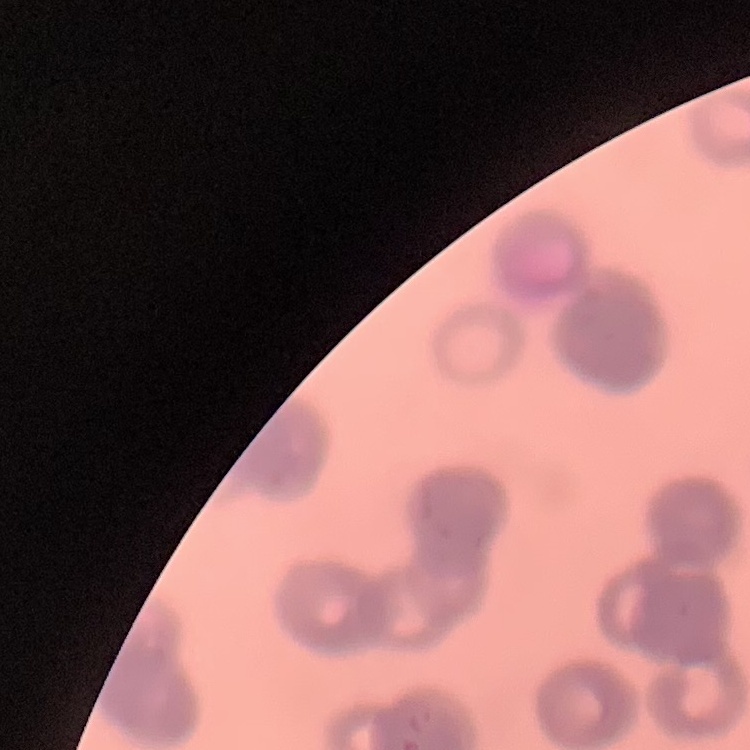
The erythrocytes show rouleaux formation. Thin peripheral smear. One tile cut from a larger photomicrograph. Field's or Giemsa stain.